State which parasite is depicted.
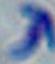

Toxoplasma gondii.

magnification = 1000x
modality = micrograph